Describe the morphology of the erythrocytes.
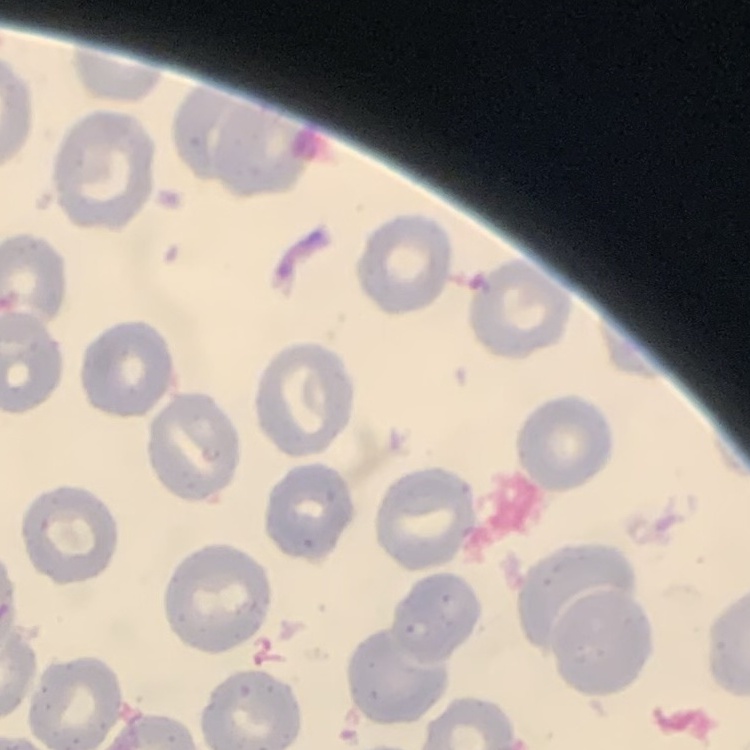
No rouleaux formation.

Summary:
  - Image type: square crop of a larger photomicrograph
  - Stain: Field's or Giemsa
  - Preparation: thin blood smear